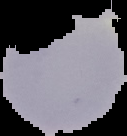
result: negative for Plasmodium parasites
preparation: thin blood smear
image_type: segmented cell region with the area outside set to black
image_size: 127×136 pixels